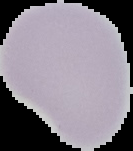
Summary:
  - Preparation: thin blood smear
  - Image type: segmented cell region with the area outside set to black
  - Malaria status: uninfected
  - Image size: 133×151 pixels